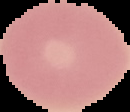

From a thin blood smear. Image is 130×112 pixels. Malaria status: uninfected. Segmented cell region on a black background.